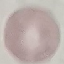

Result: no malaria parasites seen. Thin blood smear. Cell patch, automatically extracted from a larger field of view and resized to 64 × 64 pixels. Photographed with a smartphone camera at the microscope eyepiece. Giemsa-stained preparation.